Give the position of every malaria parasite.
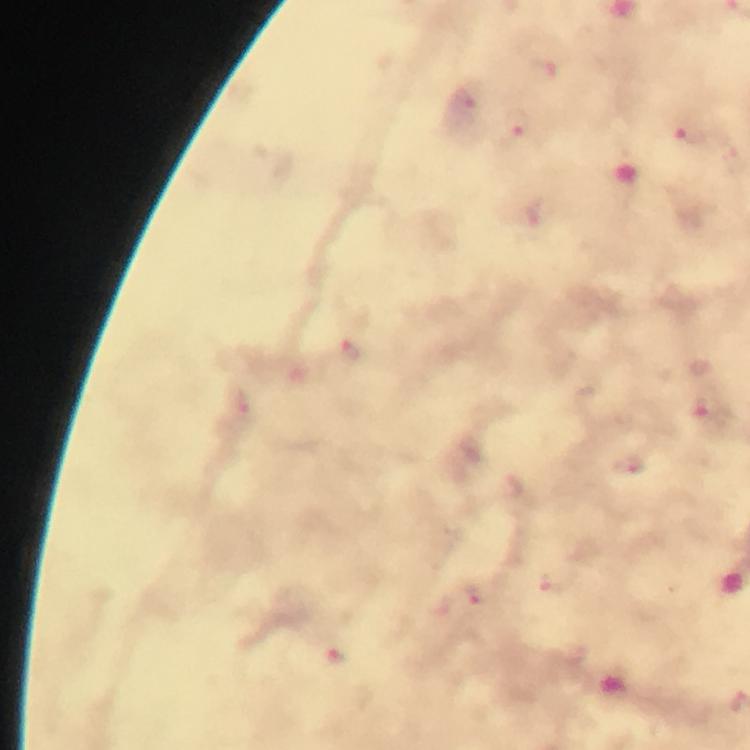
Approximate centers as (x, y) in pixels.
Malaria parasites: (544, 70), (464, 102), (519, 123), (693, 136), (354, 354), (245, 407), (630, 464), (561, 582), (473, 599), (335, 656).

Summary:
  - Preparation: thick smear
  - Cropped from: one field of view
  - Context: from a diagnostic examination for malaria
  - Magnification: 100x
  - Capture: smartphone photograph through a microscope
  - Image size: 750×750 pixels
  - Immersion oil: used
  - Stain: Giemsa